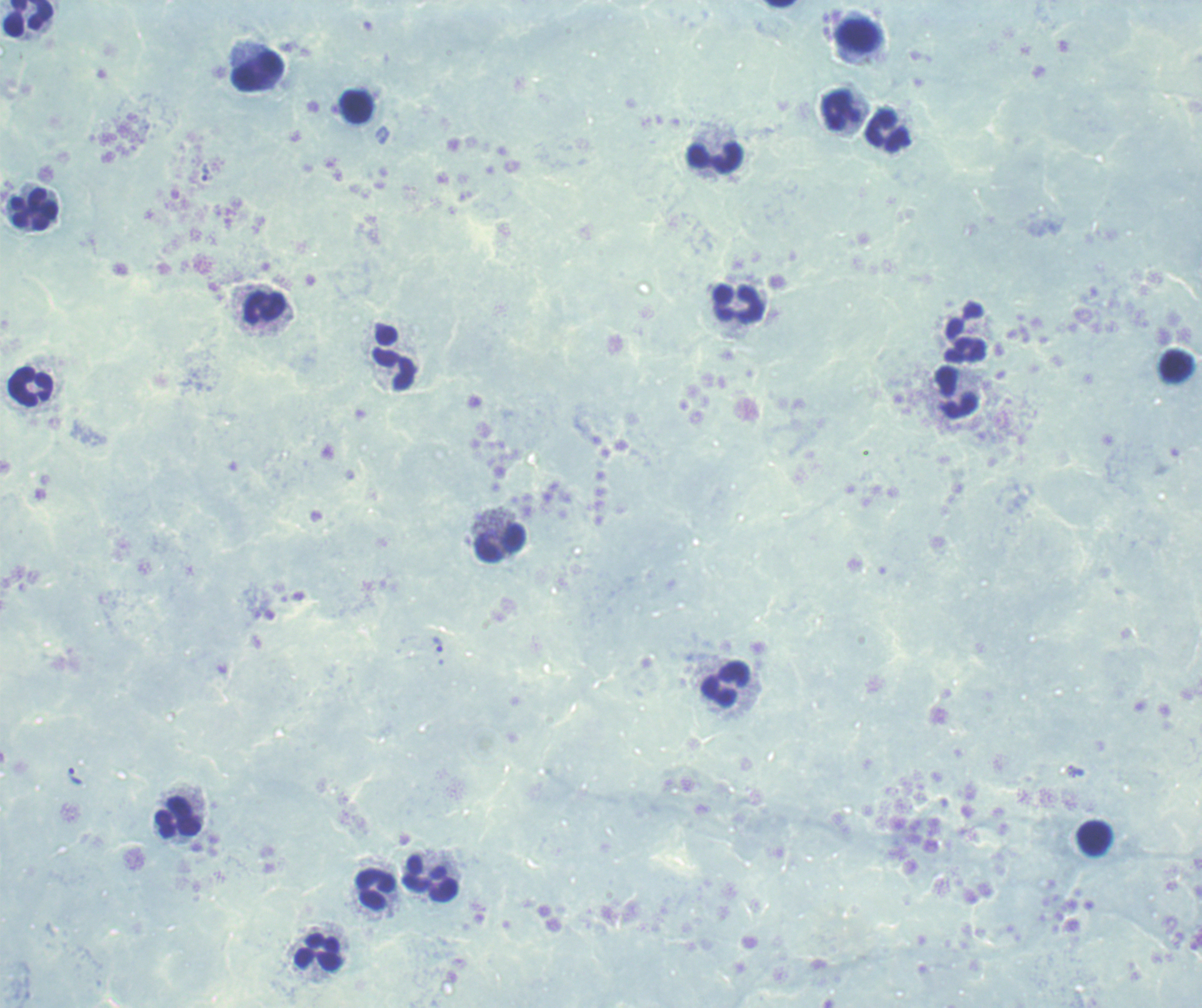

coordinate format = approximate centers as [x, y] in pixels
trophozoite locations = [207, 173], [438, 644], [76, 776]
leukocyte locations = [28, 18], [859, 33], [259, 71], [357, 107], [842, 111], [887, 128], [715, 157], [34, 210], [739, 304], [264, 307], [965, 332], [1178, 365], [395, 369], [30, 385], [957, 392], [501, 543], [726, 683], [179, 817], [1094, 838], [432, 879], [375, 888], [319, 951]
magnification = 100x
result = Plasmodium parasites detected
context = previously used in an actual diagnosis
stain = Romanowsky
image size = 1202×1008 pixels
field of view = single
background quality = poor
preparation = thick blood film